Point out each Plasmodium parasite.
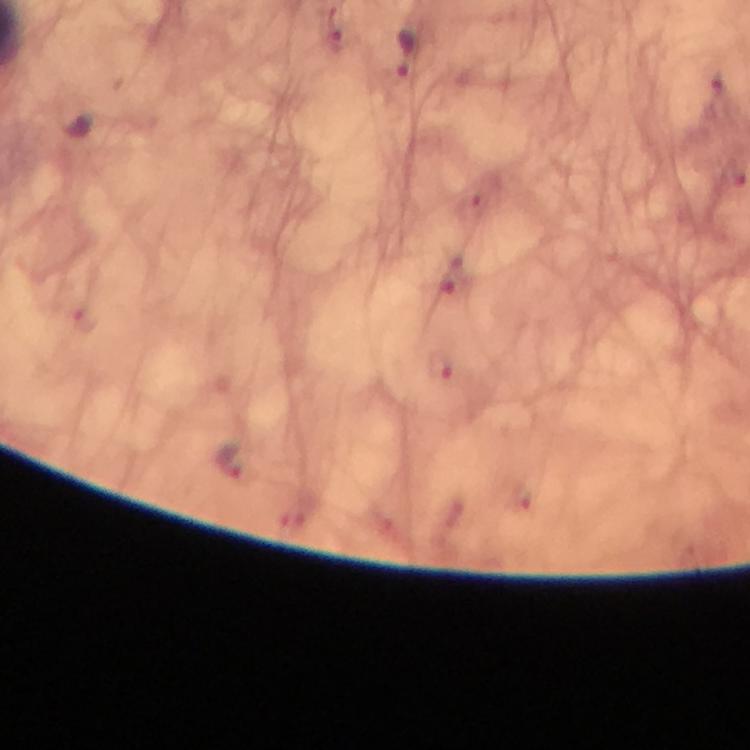
Approximate object centers, in pixels from the top-left corner.
Plasmodium parasites: (x=405, y=55).

Summary:
  - Immersion oil: used
  - Context: from a diagnostic examination for malaria
  - Capture: smartphone photograph through a microscope
  - Preparation: thick blood film
  - Image size: 750×750 pixels
  - Stain: Giemsa
  - Magnification: 100x
  - Cropped from: one field of view